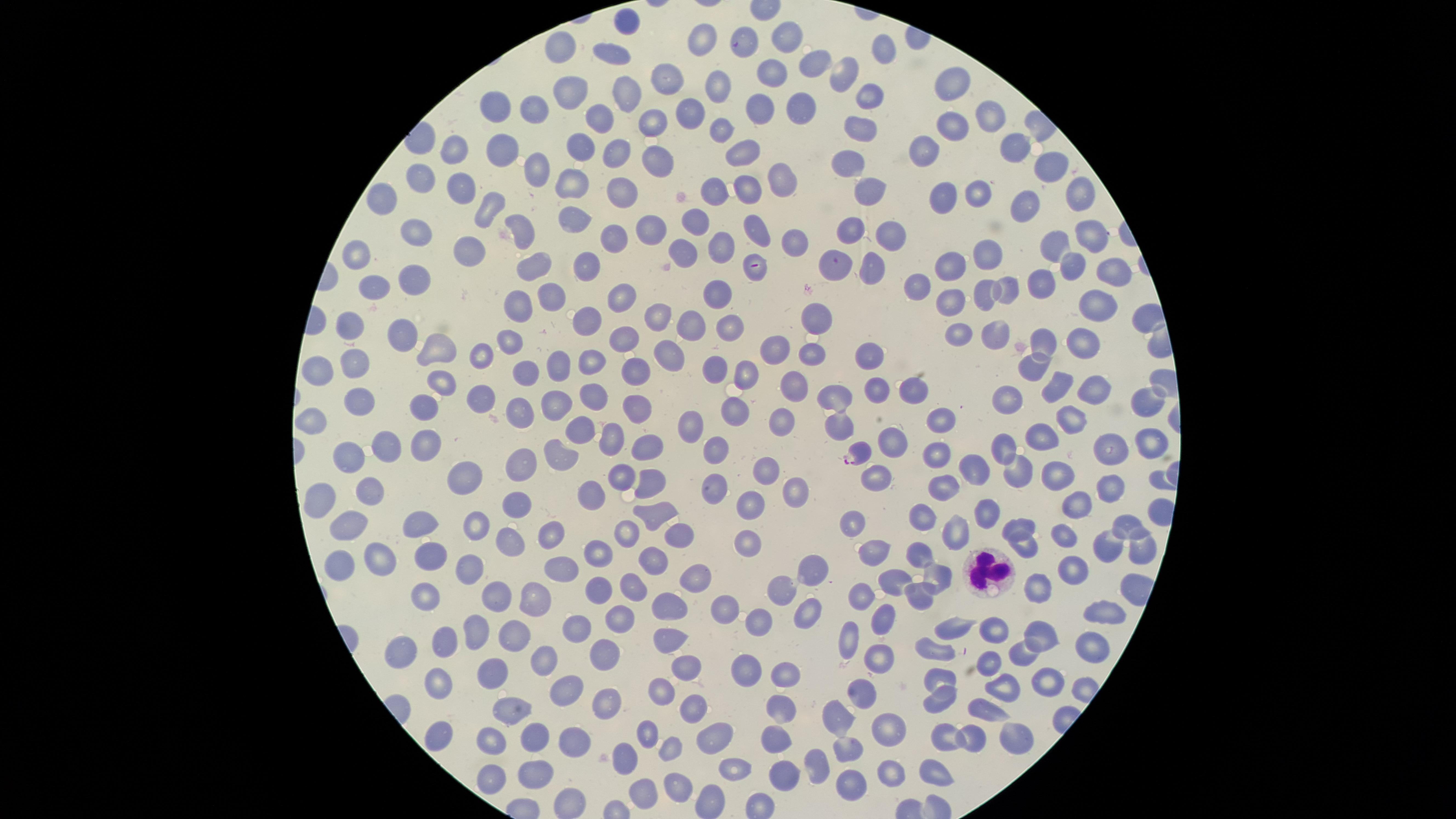

Approximate marker points as (x, y) in pixels. White blood cells: (991, 569). Parasitized red blood cells: (857, 453). Uninfected red blood cells: (625, 22), (785, 35), (703, 41), (745, 42), (557, 46), (877, 52), (612, 56), (808, 61), (769, 71), (846, 72), (661, 73), (719, 81), (951, 81), (567, 91), (624, 93), (869, 95), (502, 104), (757, 105), (798, 105), (536, 108), (690, 112), (988, 112), (599, 120), (651, 120), (953, 125), (861, 126), (719, 127), (582, 141), (498, 146), (927, 146), (616, 147), (446, 149), (741, 149), (1010, 150), (653, 156), (852, 156), (534, 168), (1052, 169), (778, 172), (425, 177), (573, 179), (459, 185), (716, 185), (864, 186), (623, 189), (985, 191), (746, 192), (1079, 193), (381, 197), (949, 199), (1026, 203), (494, 205), (576, 217), (699, 220), (852, 227), (646, 228), (892, 228), (525, 230), (1090, 230), (753, 231), (419, 234), (610, 236), (790, 237), (361, 245), (719, 247), (1054, 247), (685, 250), (983, 253), (467, 254), (875, 262), (534, 263), (589, 264), (947, 265), (1071, 266), (840, 267), (756, 270), (1103, 273), (414, 274), (919, 284), (1043, 285), (374, 287), (1009, 287), (722, 290), (980, 291), (616, 292), (548, 296), (948, 299), (1094, 305), (517, 310), (652, 316), (818, 321), (586, 324), (691, 324), (349, 325), (731, 327), (963, 331), (400, 332), (996, 336), (510, 337), (621, 338), (1041, 343), (439, 344), (1087, 346), (772, 350), (478, 351), (670, 352), (812, 352), (866, 359), (351, 362), (548, 363), (588, 364), (317, 366), (716, 366), (1035, 368), (743, 369), (633, 372), (523, 376), (444, 381), (1088, 382), (793, 384), (1053, 385), (911, 393), (588, 394), (873, 395), (1011, 395), (478, 397), (1142, 398), (355, 400), (551, 402), (635, 403), (832, 405), (519, 406), (419, 407), (734, 411), (311, 413), (783, 414), (1071, 419), (936, 421), (690, 424), (577, 427), (842, 428), (611, 435), (1041, 435), (895, 439), (1153, 441), (423, 443), (645, 444), (1002, 445), (385, 446), (1112, 450), (713, 451), (940, 454), (556, 458), (348, 459), (1023, 466), (965, 467), (619, 468), (760, 469), (527, 470), (1058, 472), (870, 474), (464, 477), (654, 480), (793, 486), (936, 486), (713, 488), (369, 489), (1112, 489), (586, 497), (319, 500), (1080, 500), (517, 505), (749, 506), (989, 509), (656, 515), (921, 516), (849, 517), (421, 522), (1122, 522), (478, 524), (1020, 525), (348, 527), (549, 528), (628, 528), (950, 528), (681, 531), (508, 540), (1067, 540), (751, 542), (875, 545), (1027, 545), (1105, 548), (594, 550), (918, 551), (1135, 552), (380, 554), (430, 555), (656, 557), (471, 564), (338, 566), (561, 569), (811, 569), (891, 572), (1072, 572), (692, 575), (938, 575), (637, 583), (1040, 585), (425, 592), (591, 593), (784, 593), (914, 596), (491, 597), (860, 597), (536, 600), (670, 607), (808, 607), (722, 611), (1098, 611), (626, 616), (880, 616), (764, 624), (951, 624), (990, 625), (474, 627), (577, 628), (515, 632), (1043, 632), (669, 636), (851, 636), (441, 644), (936, 647), (1088, 650), (606, 652), (877, 653), (395, 654), (1022, 656), (990, 661), (549, 663), (687, 665), (747, 672), (940, 672), (497, 674), (784, 674), (442, 684), (1049, 684), (1005, 686), (565, 688), (660, 688), (858, 692), (602, 697), (937, 700), (990, 709), (778, 711), (514, 712), (697, 712), (842, 718), (882, 720), (442, 728), (651, 729), (1009, 731), (949, 732), (571, 735), (712, 735), (530, 736), (774, 737), (975, 739), (494, 742), (847, 745), (671, 749), (622, 754), (740, 761), (816, 764), (535, 772), (782, 772), (886, 773), (931, 773), (490, 775), (674, 782), (855, 787), (645, 793), (571, 801). Presence: malaria parasites detected. Photographed with a smartphone camera through the microscope eyepiece. Circular visible region. Thin blood film. One field of view of the specimen. Giemsa stain. Species: Plasmodium falciparum. Image is 1456×819 pixels.